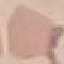
{
  "result": "negative for malaria parasites",
  "image_type": "automatically extracted cell patch, resized to 64 × 64 pixels",
  "preparation": "thin blood film",
  "stain": "Giemsa",
  "capture": "smartphone through the microscope eyepiece"
}